Locate and identify every blood parasite.
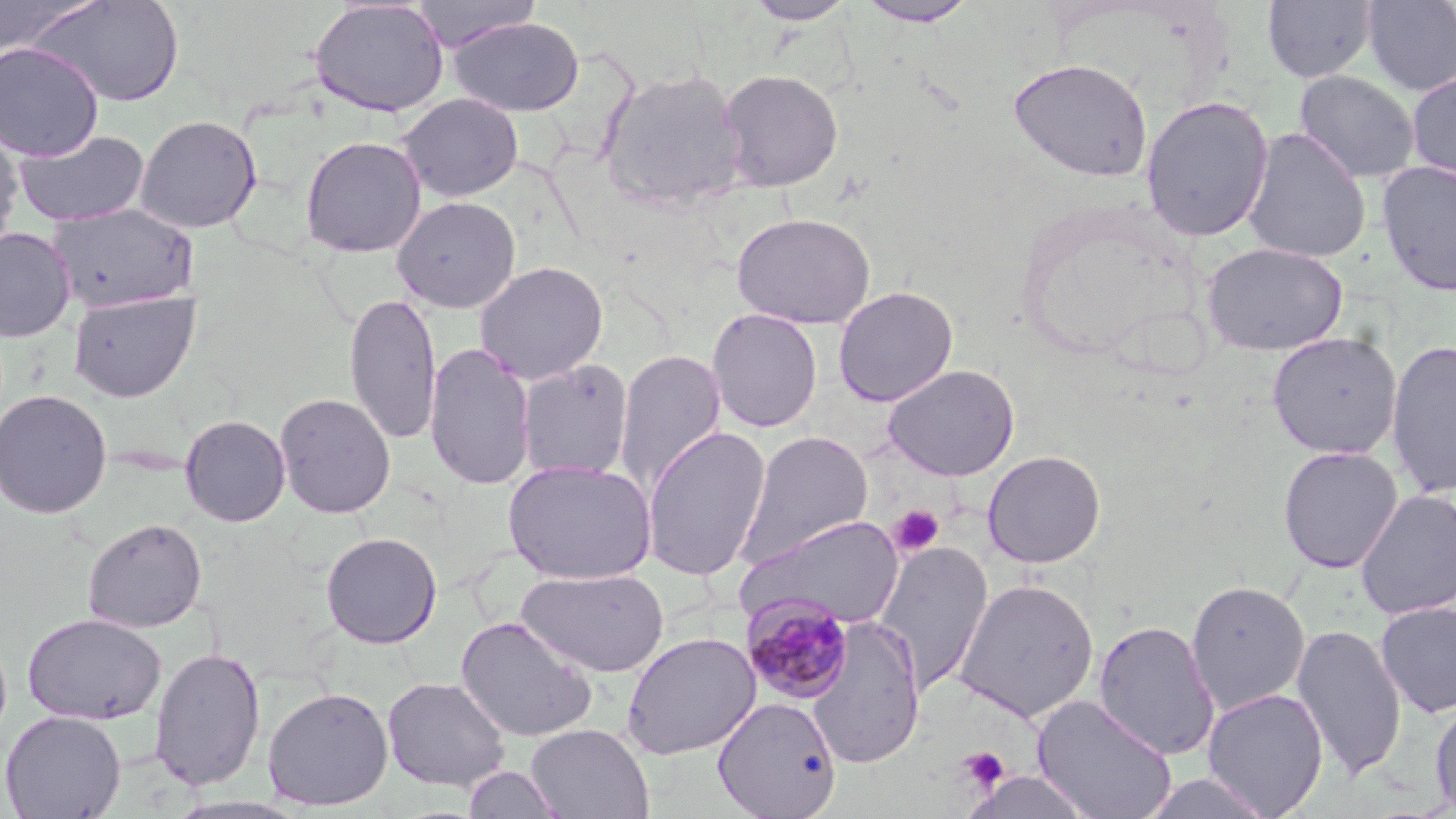
Approximate bounding boxes as [x1, y1, x2, y2] in pixels.
Plasmodium malariae-infected red blood cells: [739, 593, 855, 705].
No Plasmodium falciparum, Plasmodium ovale, Plasmodium vivax, Babesia divergens, or Trypanosoma brucei observed.

Platelet locations: [888, 503, 947, 558], [957, 746, 1011, 793]. Uninfected red blood cell locations: [0, 0, 95, 59], [27, 0, 186, 107], [411, 0, 543, 53], [745, 0, 856, 25], [1262, 0, 1377, 83], [1361, 0, 1456, 96], [309, 1, 449, 117], [856, 1, 978, 26], [449, 17, 584, 116], [0, 41, 105, 161], [1007, 57, 1154, 182], [597, 66, 747, 214], [1406, 67, 1456, 185], [718, 69, 844, 192], [1294, 70, 1420, 185], [397, 93, 523, 202], [1140, 95, 1275, 242], [134, 115, 263, 234], [0, 124, 24, 249], [1242, 127, 1371, 264], [13, 129, 151, 227], [300, 135, 427, 257], [1377, 159, 1456, 297], [392, 196, 521, 313], [47, 203, 200, 313], [730, 211, 877, 329], [0, 227, 76, 342], [1202, 242, 1347, 356], [474, 261, 609, 384], [832, 286, 958, 407], [68, 290, 201, 402], [344, 291, 441, 444], [707, 308, 823, 433], [1267, 331, 1402, 459], [1386, 339, 1456, 498], [424, 342, 536, 491], [613, 348, 727, 499], [516, 359, 634, 481], [882, 364, 1020, 481], [0, 389, 113, 519], [274, 392, 396, 519], [179, 414, 291, 527], [641, 424, 772, 581], [737, 431, 874, 568], [1278, 445, 1403, 574], [981, 449, 1107, 568], [503, 458, 658, 584], [1355, 489, 1456, 621], [739, 513, 906, 631], [82, 518, 208, 633], [320, 532, 443, 649], [874, 541, 994, 698], [517, 567, 671, 677], [952, 578, 1100, 724], [1186, 579, 1310, 715], [1375, 601, 1456, 718], [22, 612, 167, 726], [456, 615, 600, 745], [807, 617, 926, 768], [1093, 620, 1220, 760], [1291, 623, 1406, 781], [621, 630, 761, 760], [149, 645, 267, 791], [383, 677, 511, 792], [262, 686, 393, 811], [1202, 688, 1329, 818], [1033, 695, 1177, 819], [713, 696, 841, 818], [1429, 696, 1456, 818], [0, 710, 126, 819], [526, 723, 654, 819], [462, 765, 564, 818], [963, 769, 1095, 819], [1140, 771, 1275, 818], [165, 795, 314, 819]. Slide-level diagnosis: Plasmodium malariae. May-Grünwald-Giemsa stain. Thin blood film. Light microscopy. Image is 1456×819 pixels. Single field of view. Captured at 1000x magnification.